Describe the morphology of the erythrocytes.
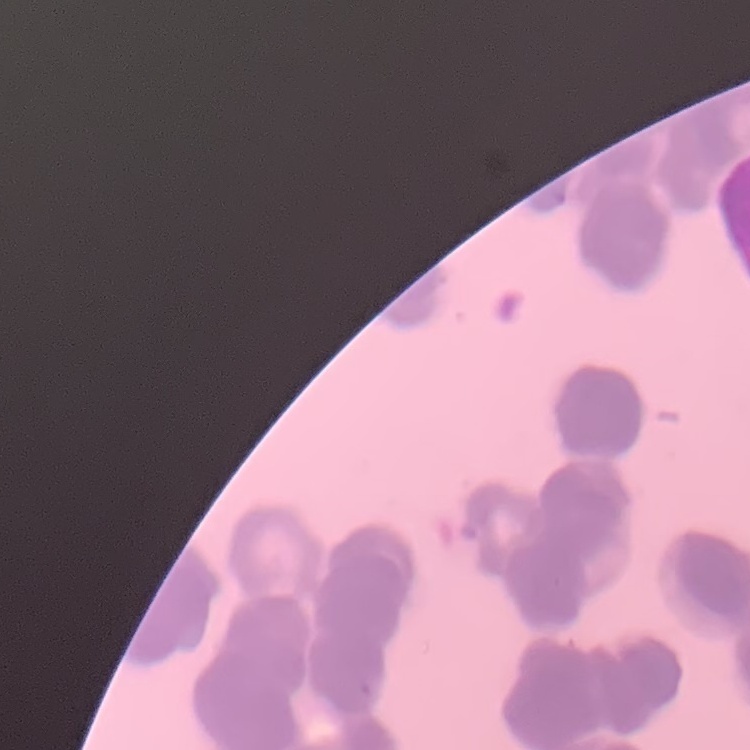
They show rouleaux formation.

Field's or Giemsa stain. One tile cut from a larger photomicrograph. Thin blood smear.